Describe the morphology of the erythrocytes.
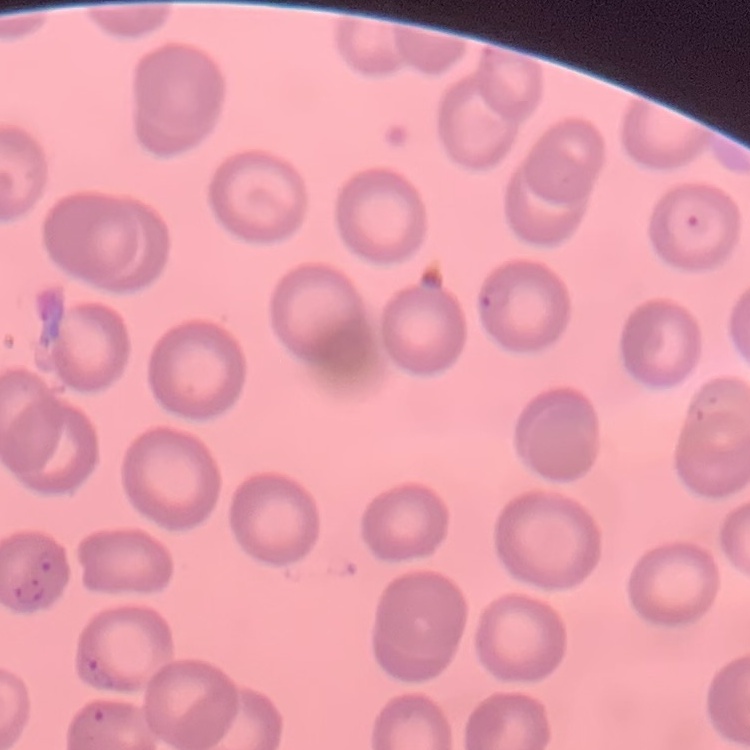

They show no rouleaux formation.

Square crop of a larger photomicrograph. Thin peripheral smear. Stained with either Field's or Giemsa.